State which parasite is depicted.
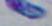

Toxoplasma gondii.

Summary:
  - Modality: micrograph
  - Magnification: 1000x